Describe the morphology of the red blood cells.
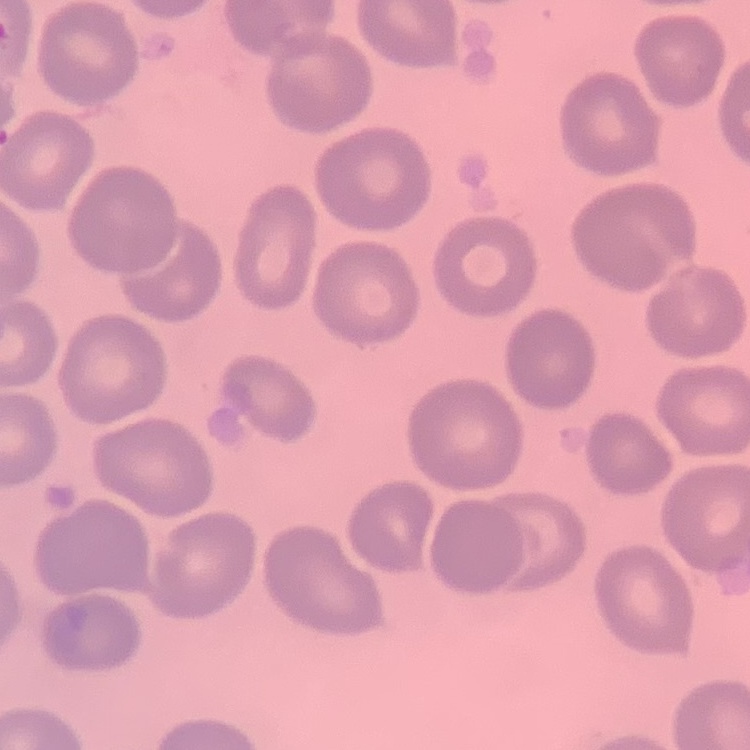
They show no rouleaux formation.

image type = square crop of a larger photomicrograph
stain = Field's or Giemsa
preparation = thin blood smear